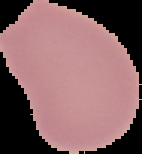
preparation = thin blood film
image type = segmented cell region with the area outside set to black
image size = 142×154 pixels
malaria status = uninfected